Find each parasitized red blood cell.
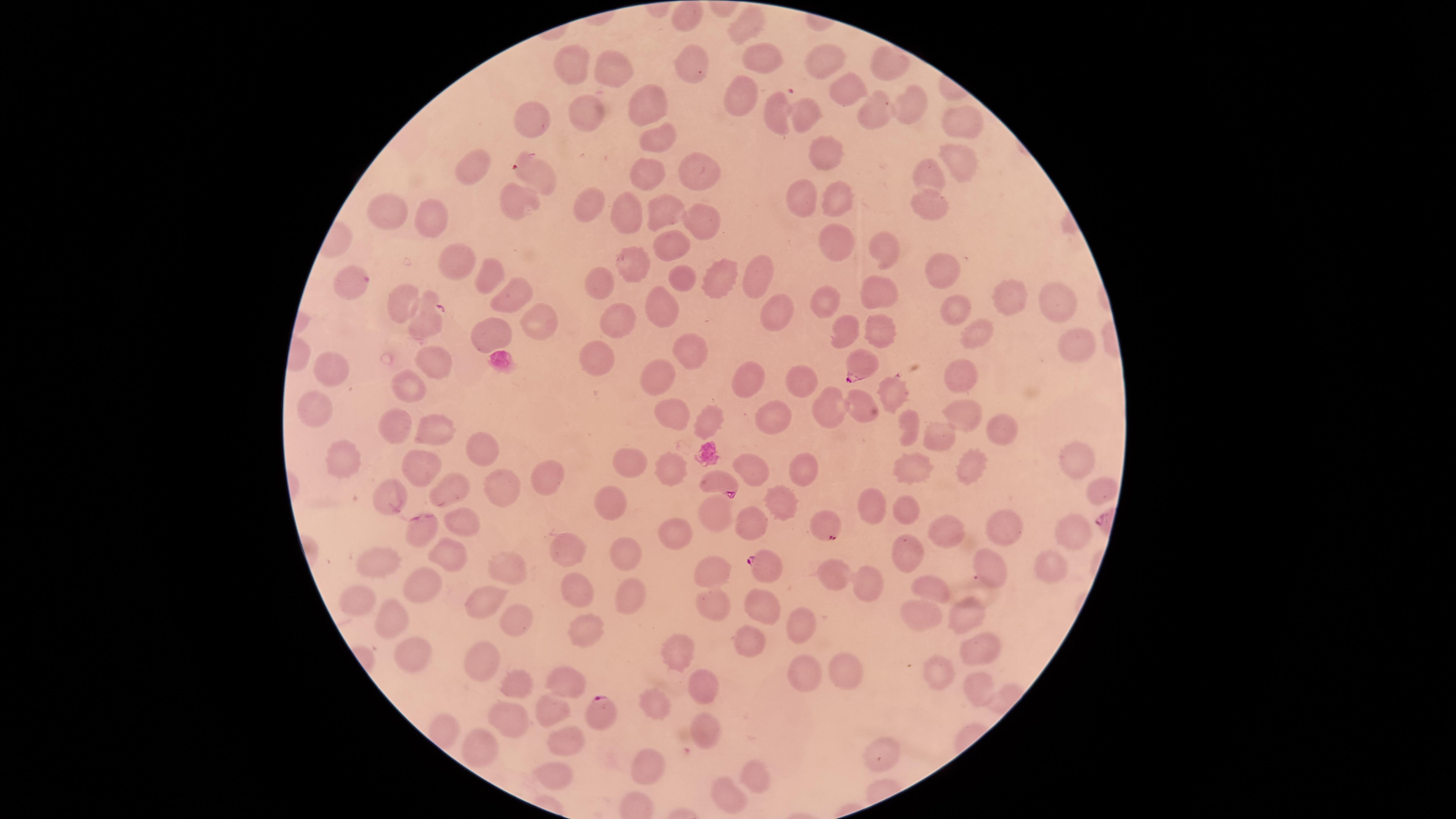
Approximate marker points as (x, y) in pixels.
Parasitized red blood cells: (427, 321), (858, 368), (716, 481), (826, 525), (770, 570), (596, 714).

Approximate marker points as (x, y) in pixels. Uninfected red blood cells: (689, 18), (748, 19), (823, 58), (767, 60), (689, 62), (581, 66), (613, 72), (851, 90), (743, 95), (649, 99), (909, 108), (880, 111), (594, 114), (806, 114), (770, 116), (961, 123), (532, 124), (656, 134), (825, 152), (962, 160), (479, 169), (531, 169), (933, 172), (648, 173), (701, 174), (519, 195), (839, 197), (930, 198), (803, 200), (599, 206), (661, 212), (383, 213), (436, 213), (622, 213), (697, 213), (835, 241), (885, 243), (676, 244), (451, 261), (635, 261), (944, 270), (483, 272), (759, 273), (680, 276), (722, 276), (350, 286), (606, 286), (512, 289), (884, 297), (1005, 298), (401, 300), (1057, 300), (826, 304), (666, 305), (948, 305), (779, 312), (545, 318), (627, 320), (498, 327), (883, 330), (982, 331), (842, 333), (1079, 342), (599, 354), (701, 356), (427, 364), (959, 372), (334, 373), (663, 373), (803, 376), (742, 381), (407, 388), (897, 395), (316, 408), (855, 409), (672, 414), (968, 414), (773, 415), (714, 419), (908, 425), (396, 428), (939, 430), (1003, 430), (437, 432), (482, 449), (1081, 460), (624, 464), (414, 465), (340, 466), (906, 466), (967, 466), (796, 467), (666, 472), (754, 472), (546, 480), (387, 488), (443, 488), (499, 488), (1088, 490), (605, 506), (880, 506), (780, 508), (902, 511), (460, 516), (713, 516), (748, 522), (1004, 530), (1063, 531), (673, 532), (944, 533), (419, 534), (559, 546), (619, 549), (908, 553), (448, 555), (377, 558), (994, 564), (1045, 569), (507, 571), (714, 572), (839, 575), (869, 582), (418, 584), (577, 584), (938, 590), (356, 593), (628, 596), (478, 597), (760, 601), (719, 605), (921, 609), (969, 614), (386, 618), (508, 619), (803, 627), (578, 634), (751, 635), (978, 643), (410, 647), (680, 651), (486, 659), (797, 667), (933, 667), (840, 671), (558, 679), (519, 682), (696, 684), (973, 685), (657, 696), (546, 711), (499, 715), (697, 727), (563, 742), (487, 744), (883, 750), (651, 768), (551, 773), (752, 776), (728, 796). One field of view of the specimen. Photographed with a smartphone camera through the microscope eyepiece. Thin smear of blood. Image is 1456×819 pixels. Giemsa-stained preparation. Circular visible region. Species: Plasmodium falciparum.